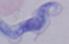

Summary:
  - Modality: micrograph
  - Identification: trypanosome
  - Magnification: 1000x